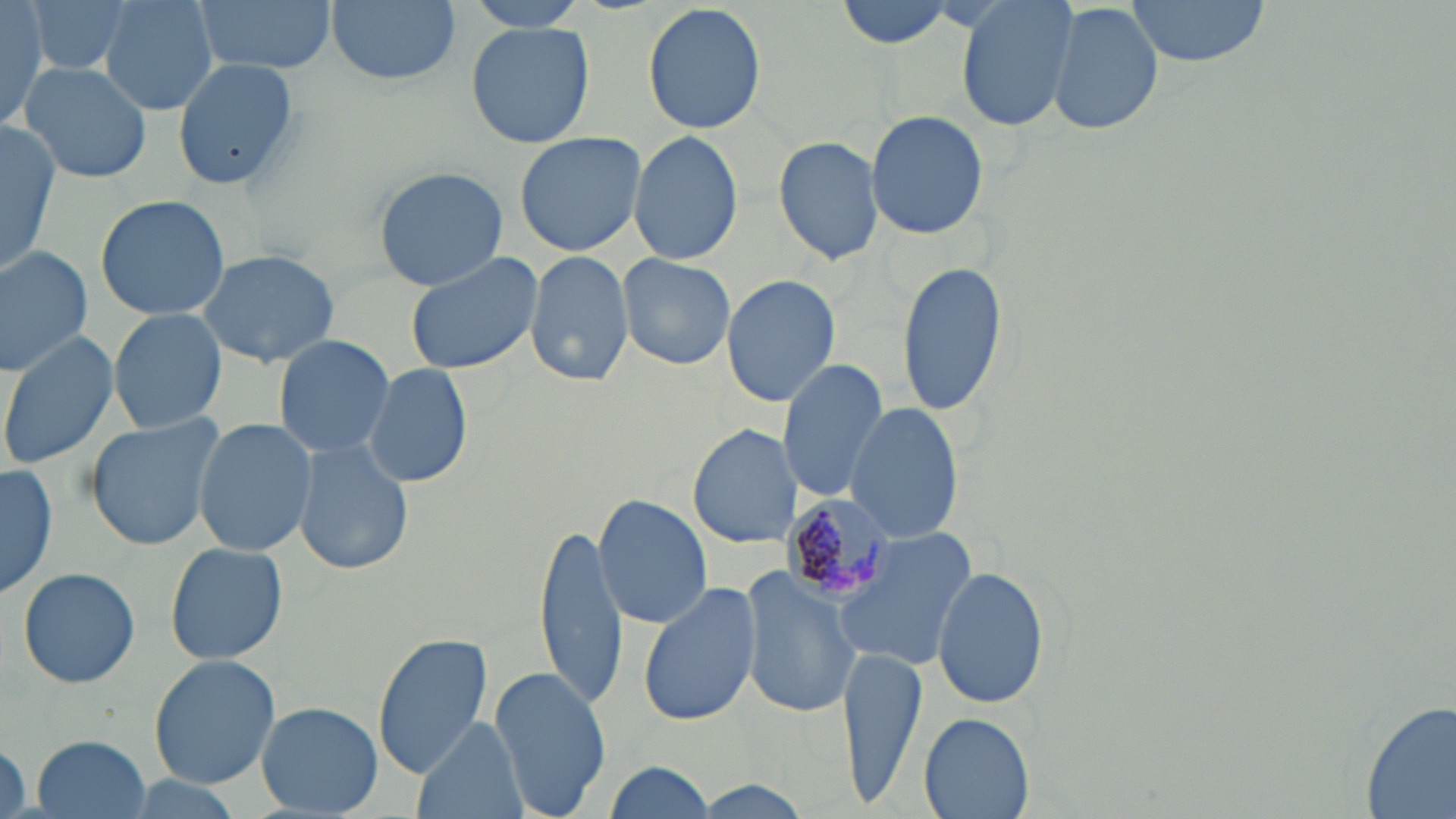
Approximate bounding boxes as (x1,y1)-(x2,y2) corner pairs in pixels. Plasmodium malariae-infected red blood cell locations: (781,494)-(904,603). Uninfected red blood cell locations: (25,0)-(138,79), (98,0)-(218,116), (194,0)-(337,77), (324,0)-(462,87), (462,0)-(593,32), (835,0)-(957,49), (954,0)-(1080,133), (1121,0)-(1274,69), (0,1)-(54,130), (1047,1)-(1164,136), (643,3)-(768,137), (466,21)-(595,149), (171,55)-(302,195), (17,60)-(152,183), (865,109)-(991,242), (0,123)-(60,279), (513,131)-(649,258), (628,131)-(743,264), (773,135)-(883,265), (374,166)-(509,290), (94,194)-(230,320), (0,245)-(92,377), (525,247)-(632,389), (196,248)-(341,367), (405,249)-(543,375), (619,253)-(736,370), (896,258)-(1008,414), (722,273)-(840,407), (109,308)-(225,432), (0,331)-(118,470), (273,335)-(395,461), (777,356)-(888,503), (364,362)-(473,488), (844,401)-(964,542), (81,413)-(228,550), (192,418)-(316,555), (688,425)-(801,549), (294,439)-(413,576), (0,463)-(58,602), (592,495)-(711,628), (533,522)-(629,708), (833,527)-(980,670), (163,541)-(290,665), (929,561)-(1052,710), (17,568)-(141,688), (742,569)-(861,719), (638,582)-(761,728), (371,633)-(497,776), (840,644)-(929,811), (148,654)-(280,790), (489,665)-(613,818), (1359,695)-(1456,819), (257,702)-(382,817), (920,712)-(1035,818), (411,717)-(526,819), (29,734)-(154,818), (2,739)-(29,819), (603,761)-(718,819), (114,775)-(248,817), (691,780)-(814,815). Slide-level diagnosis: Plasmodium malariae. Thin blood smear. Optical microscopy. 1000x magnification. May-Grünwald-Giemsa-stained preparation. One field of a larger specimen. Image is 1456×819 pixels.